Comment on the morphology of the erythrocytes.
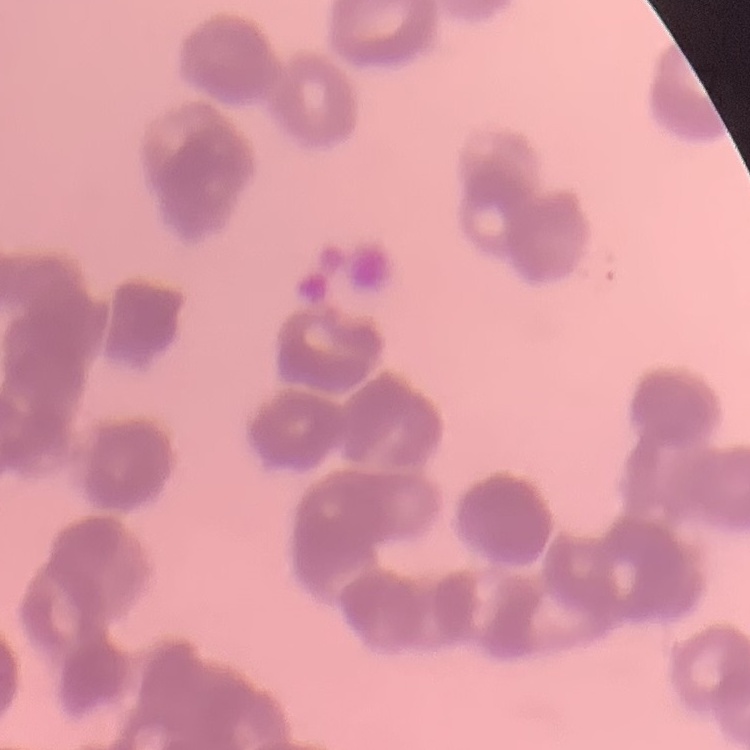
Rouleaux formation.

image type = square crop of a larger photomicrograph
preparation = thin peripheral smear
stain = Field's or Giemsa